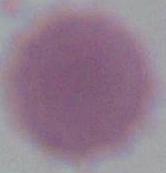

{
  "magnification": "1000x",
  "modality": "micrograph",
  "identification": "erythrocyte"
}